Assess the morphology of the erythrocytes.
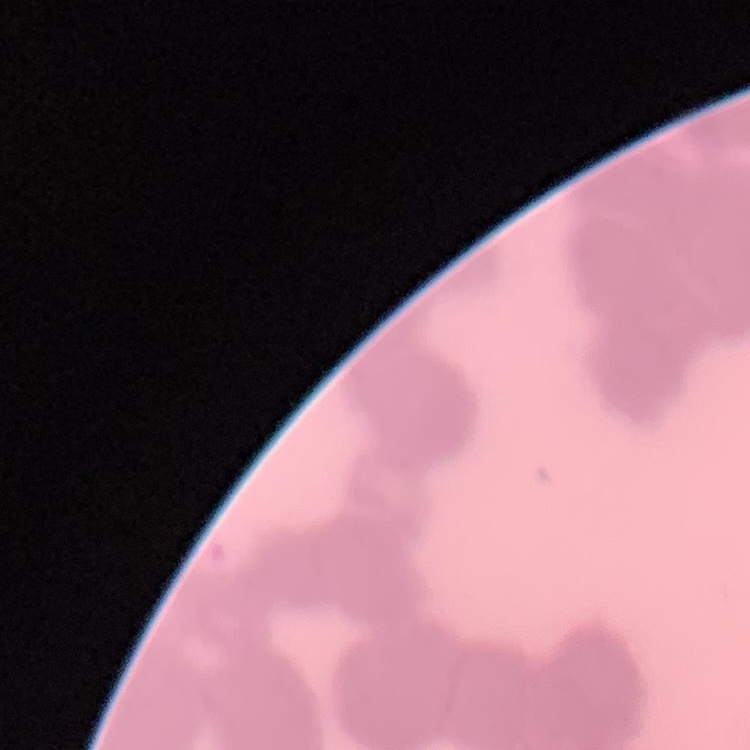

They show rouleaux formation.

stain = Field's or Giemsa
preparation = thin blood film
image type = square crop of a larger photomicrograph